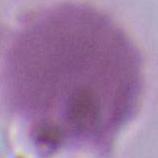
Summary:
  - Modality: photomicrograph
  - Identification: erythrocyte
  - Magnification: 1000x